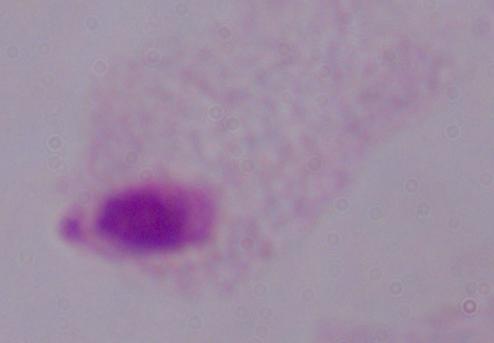

A trichomonad is shown. Photomicrograph. Captured at 1000x magnification.